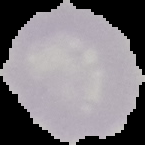 Image is 145×145 pixels. Result: negative for malaria parasites. The area outside the segmented cell region is set to black. From a thin blood film.